Describe the morphology of the red blood cells.
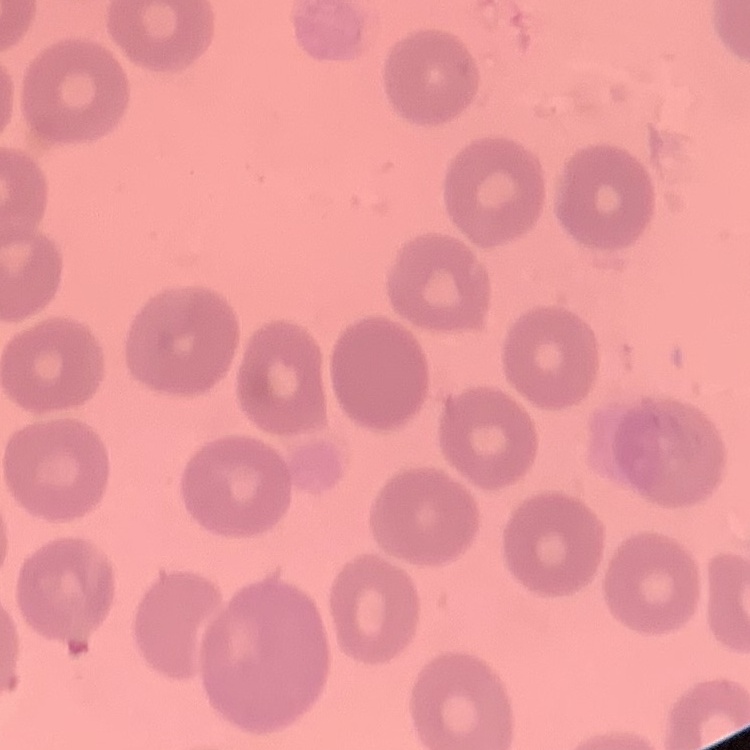

No rouleaux formation.

Summary:
  - Preparation: thin blood smear
  - Image type: square crop of a larger photomicrograph
  - Stain: Field's or Giemsa